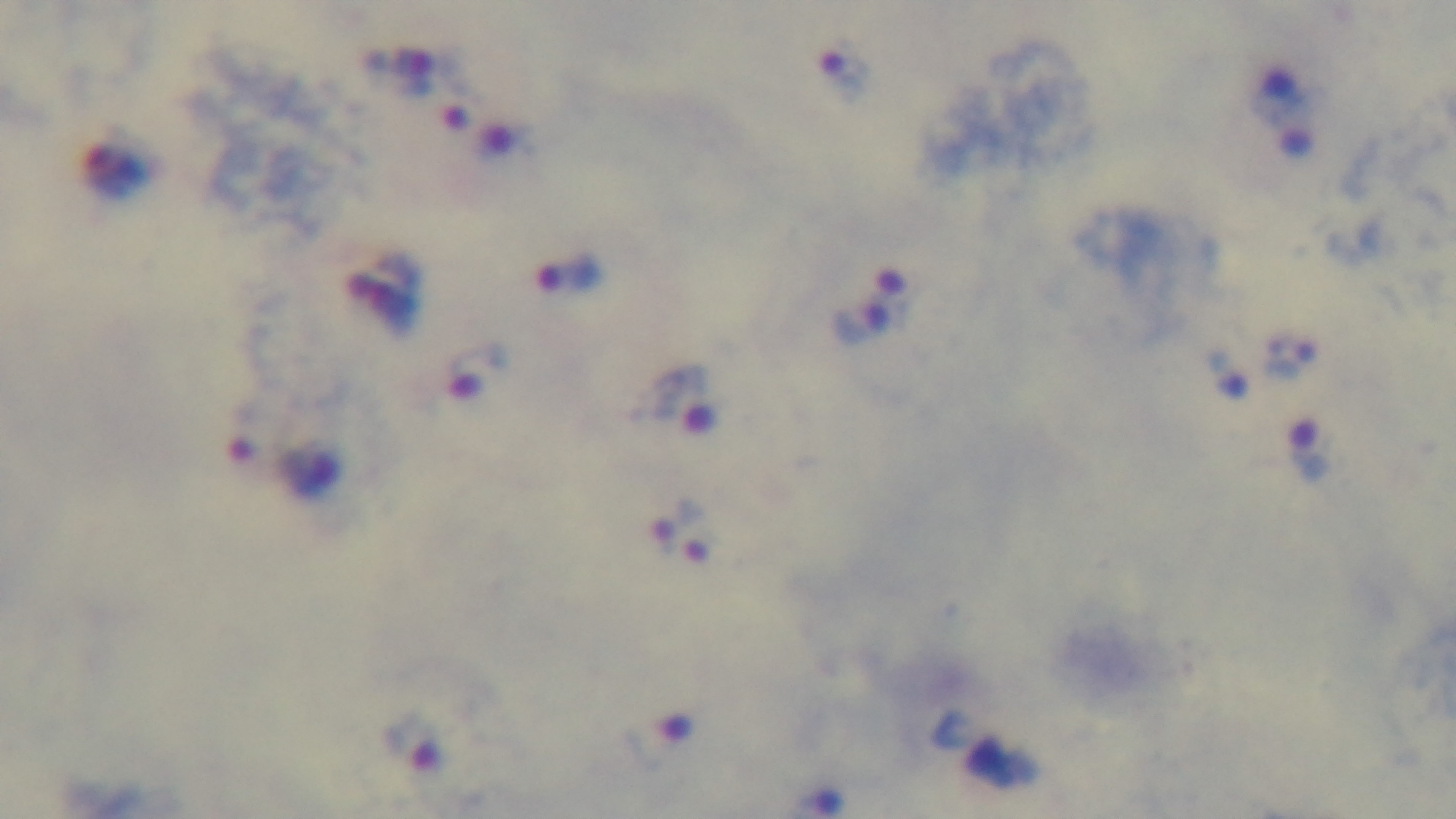 100x oil-immersion objective. Mounted 4K digital camera. Photomicrograph. Malaria status: positive. Preparation: thick. One field from the slide. Giemsa-stained.